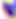
identification = Toxoplasma gondii
magnification = 400x
modality = photomicrograph